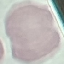
Summary:
  - Result: no malaria parasites seen
  - Stain: Giemsa
  - Preparation: thin blood film
  - Image type: automatically extracted cell patch, resized to 64 × 64 pixels
  - Capture: smartphone through the microscope eyepiece